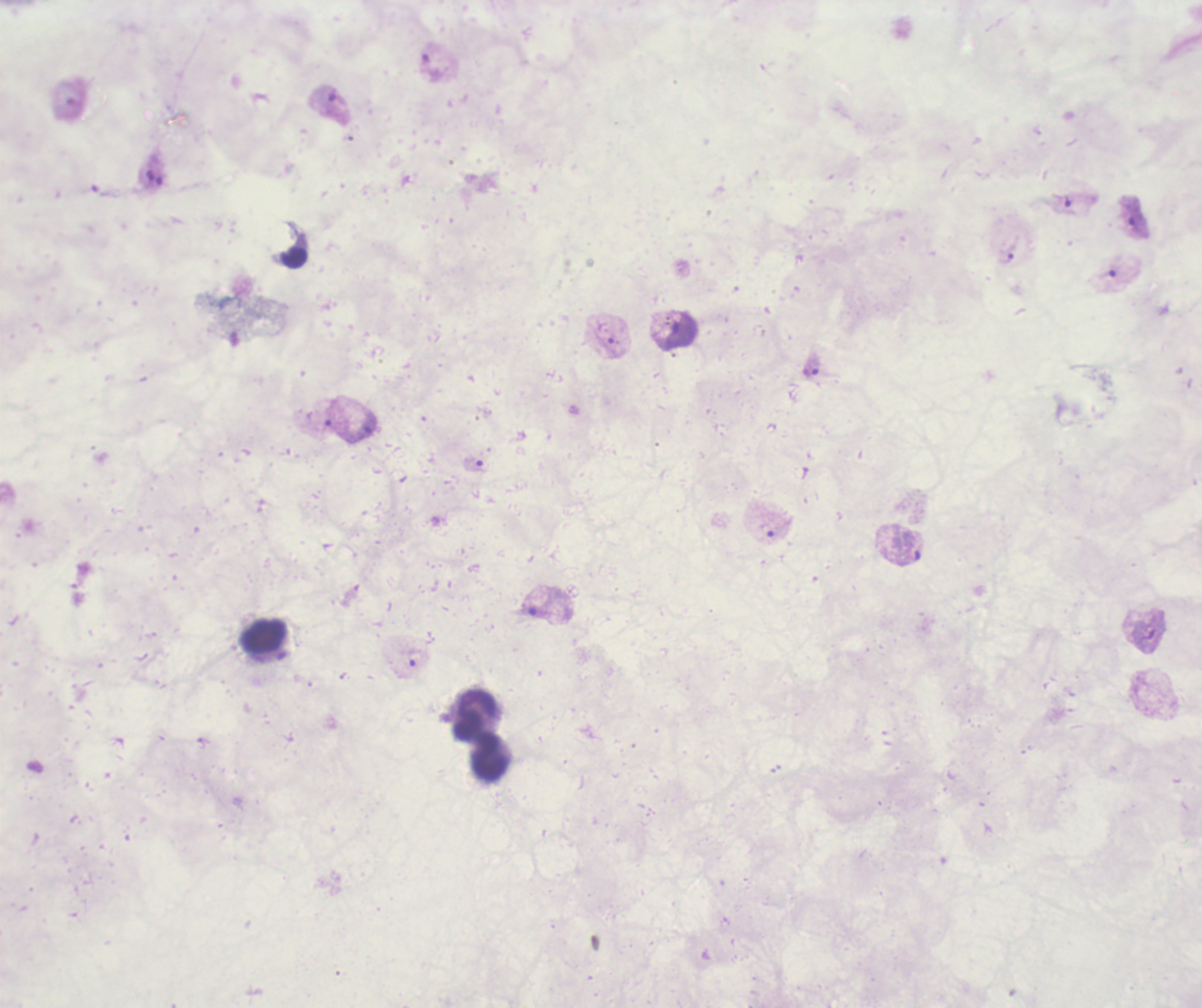
Approximate object centers, in pixels from the top-left corner. Trophozoite locations: (x=326, y=101), (x=1064, y=205), (x=1134, y=215), (x=1009, y=252), (x=1105, y=277), (x=679, y=333), (x=813, y=366), (x=364, y=429), (x=475, y=464), (x=906, y=558), (x=539, y=606), (x=413, y=659). Leukocyte locations: (x=262, y=636), (x=473, y=715), (x=492, y=757). Result: malaria parasites detected. Previously used in an actual diagnosis. Image is 1202×1008 pixels. Captured at 100x magnification. Romanowsky stain. One field from this slide. Thick smear of blood. Background quality: unsatisfactory.